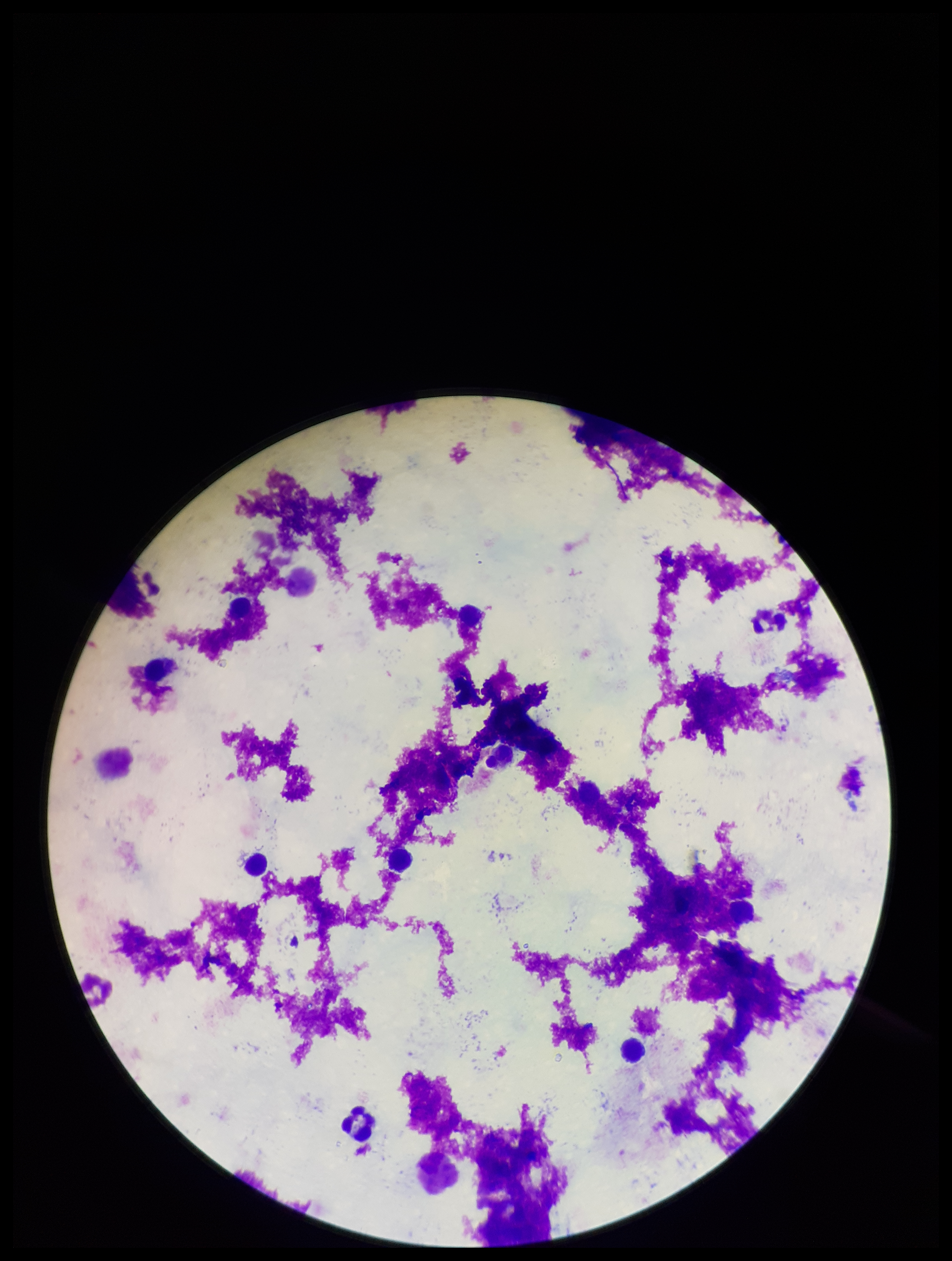 Giemsa stain. Image is 952×1261 pixels. Smartphone photograph taken through the eyepiece of a microscope. Leukocyte count: 9. Patient malaria status: negative. Preparation: thick smear. One field from this slide. Plasmodium parasites: none identified. Parasite count: 0.